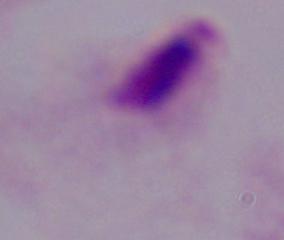
A trichomonad is seen. Photomicrograph. 1000x magnification.